Give the preparation type.
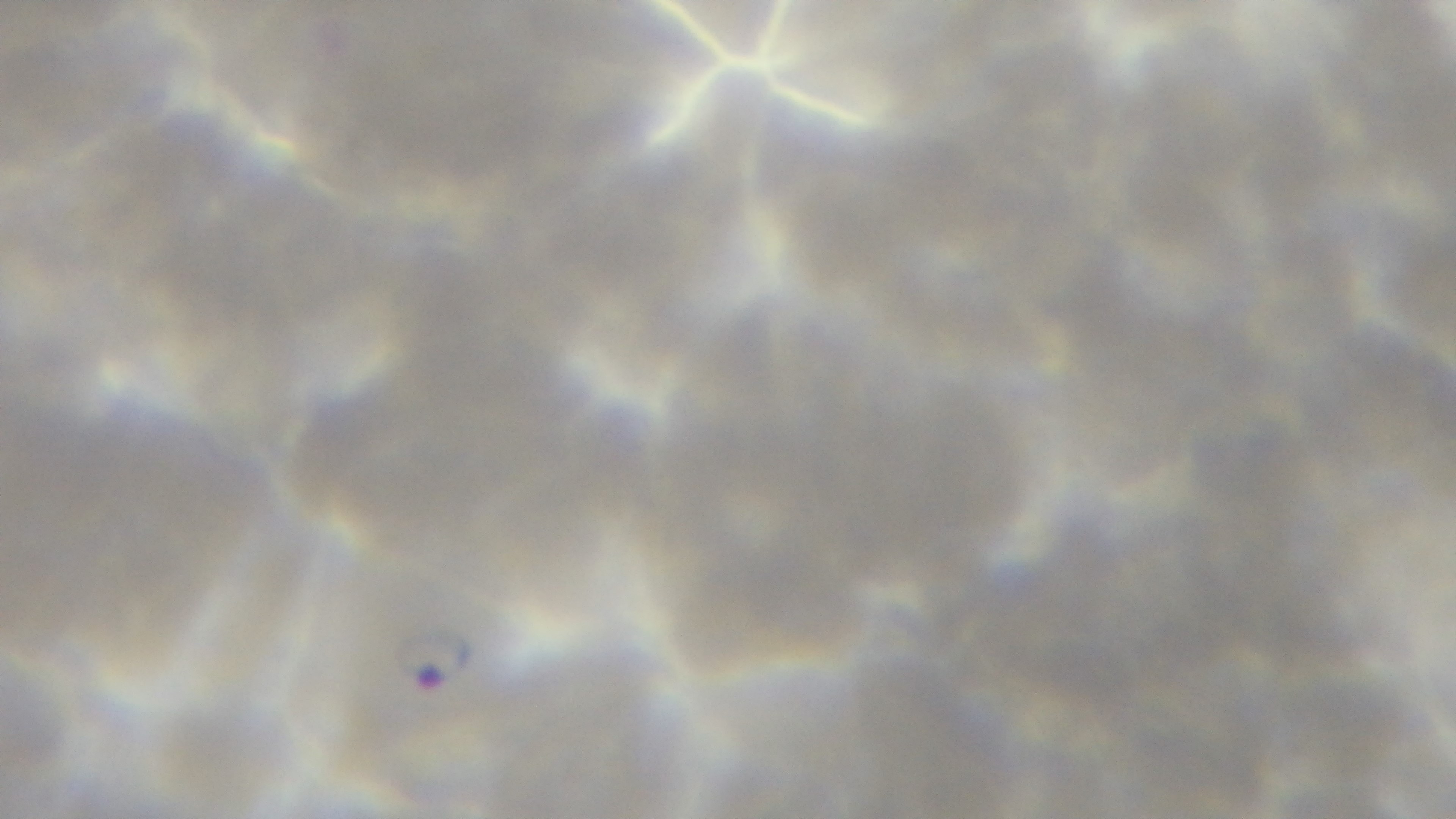

A thin smear.

Giemsa stain. Oil-immersion objective, 100x. Photomicrograph. Single field of view. Captured with a mounted 4K digital camera. Malaria status: infected.